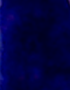
magnification: 1000x
identification: leukocyte
modality: micrograph